Assess this cell for malaria.
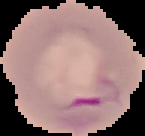

It is parasitized.

{
  "image_size": "145×136 pixels",
  "image_type": "segmented cell region on a black background",
  "preparation": "thin blood film"
}